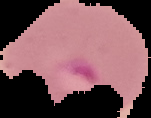 From a thin blood smear. Cell region segmented out of the field of view; the surrounding area is masked to black. Image is 151×118 pixels. Malaria status: parasitized.